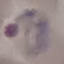

result = malaria parasites identified
image type = automatically extracted cell patch, resized to 64 × 64 pixels
stain = Giemsa
preparation = thin smear
capture = smartphone through the microscope eyepiece